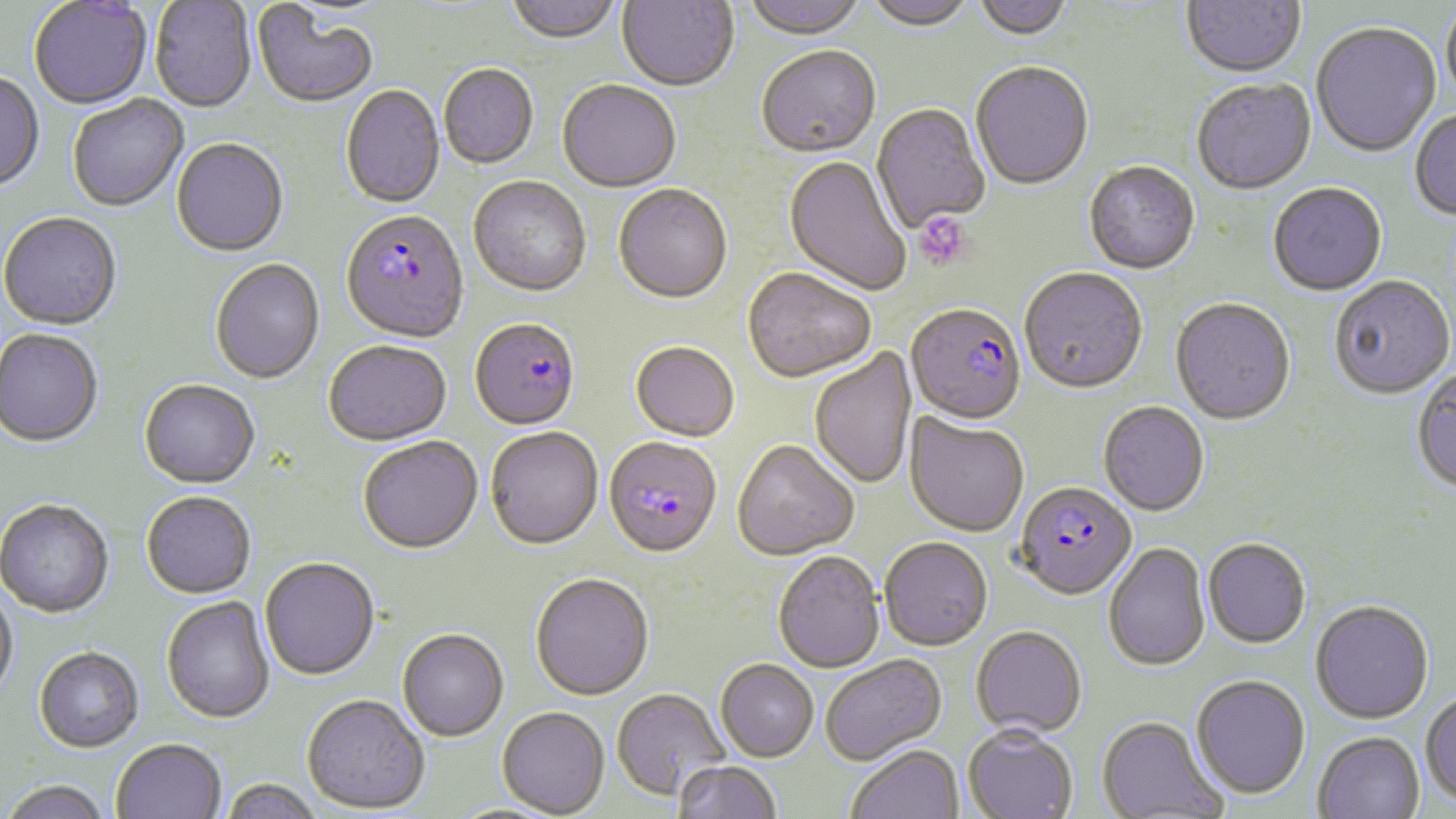

Summary:
  - Coordinate format: approximate bounding boxes as [x1, y1, x2, y2] in pixels
  - Uninfected red blood cell locations: [504, 0, 621, 47], [617, 0, 739, 93], [740, 0, 867, 42], [863, 0, 976, 34], [973, 0, 1074, 43], [1181, 0, 1306, 81], [29, 1, 152, 111], [150, 1, 256, 114], [1442, 2, 1456, 117], [253, 5, 378, 109], [1311, 24, 1441, 159], [757, 48, 881, 160], [971, 63, 1094, 192], [439, 65, 538, 170], [0, 73, 45, 193], [1192, 81, 1316, 197], [557, 82, 681, 194], [341, 86, 445, 210], [68, 96, 189, 212], [872, 104, 990, 233], [1410, 110, 1456, 222], [171, 139, 288, 258], [783, 156, 910, 298], [1084, 163, 1200, 276], [469, 178, 591, 299], [1268, 185, 1387, 298], [614, 186, 732, 306], [0, 215, 122, 332], [210, 260, 325, 385], [742, 269, 876, 384], [1019, 270, 1148, 396], [1330, 277, 1455, 401], [1170, 300, 1296, 427], [0, 331, 102, 448], [324, 342, 452, 448], [630, 343, 740, 444], [810, 347, 918, 490], [1411, 368, 1456, 496], [139, 381, 259, 490], [1099, 402, 1209, 517], [905, 413, 1029, 538], [485, 429, 604, 552], [358, 437, 483, 556], [732, 442, 858, 562], [141, 493, 256, 600], [0, 501, 114, 620], [880, 538, 992, 652], [1203, 539, 1310, 650], [1103, 542, 1210, 673], [772, 552, 884, 673], [260, 558, 380, 682], [530, 574, 654, 702], [0, 582, 19, 703], [161, 597, 275, 724], [1311, 601, 1433, 725], [970, 626, 1086, 738], [397, 630, 508, 743], [34, 648, 144, 755], [821, 654, 947, 766], [715, 660, 818, 762], [1191, 676, 1311, 799], [612, 689, 729, 801], [1421, 691, 1456, 807], [302, 695, 430, 815], [496, 707, 609, 817], [1096, 715, 1226, 818], [962, 726, 1079, 819], [1313, 732, 1425, 819], [111, 740, 227, 819], [846, 746, 964, 819], [673, 761, 781, 819], [220, 780, 323, 819], [1, 782, 113, 819]
  - Platelet locations: [915, 212, 973, 271]
  - Plasmodium falciparum-infected red blood cell locations: [341, 211, 470, 346], [906, 306, 1026, 428], [470, 320, 580, 432], [604, 438, 723, 561], [1015, 483, 1137, 601]
  - Slide-level diagnosis: Plasmodium falciparum
  - Magnification: 1000x
  - Modality: optical microscopy
  - Image size: 1456×819 pixels
  - Preparation: thin blood smear
  - Stain: May-Grünwald-Giemsa
  - Field of view: single